Assess the morphology of the erythrocytes.
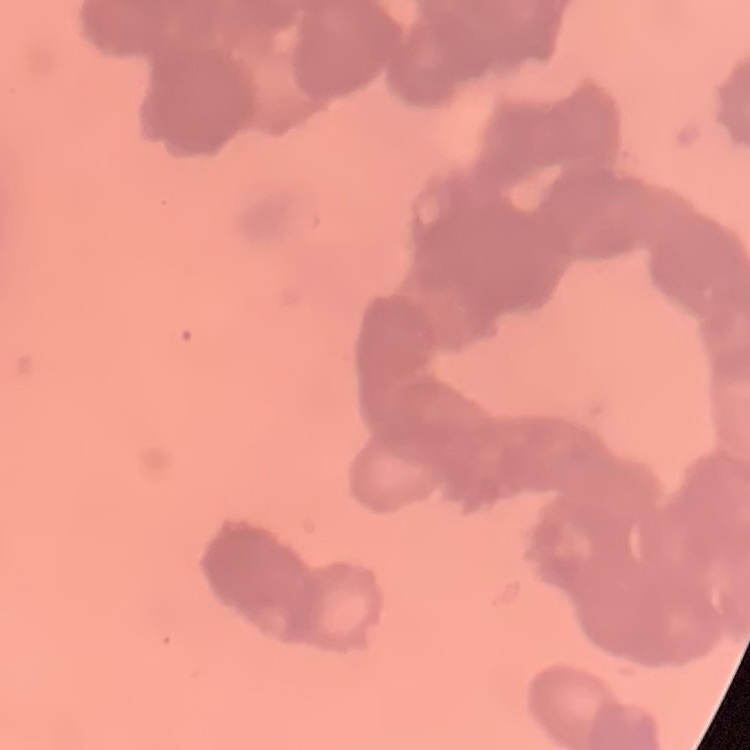

They show rouleaux formation.

image type = square crop of a larger photomicrograph
preparation = thin blood film
stain = Field's or Giemsa